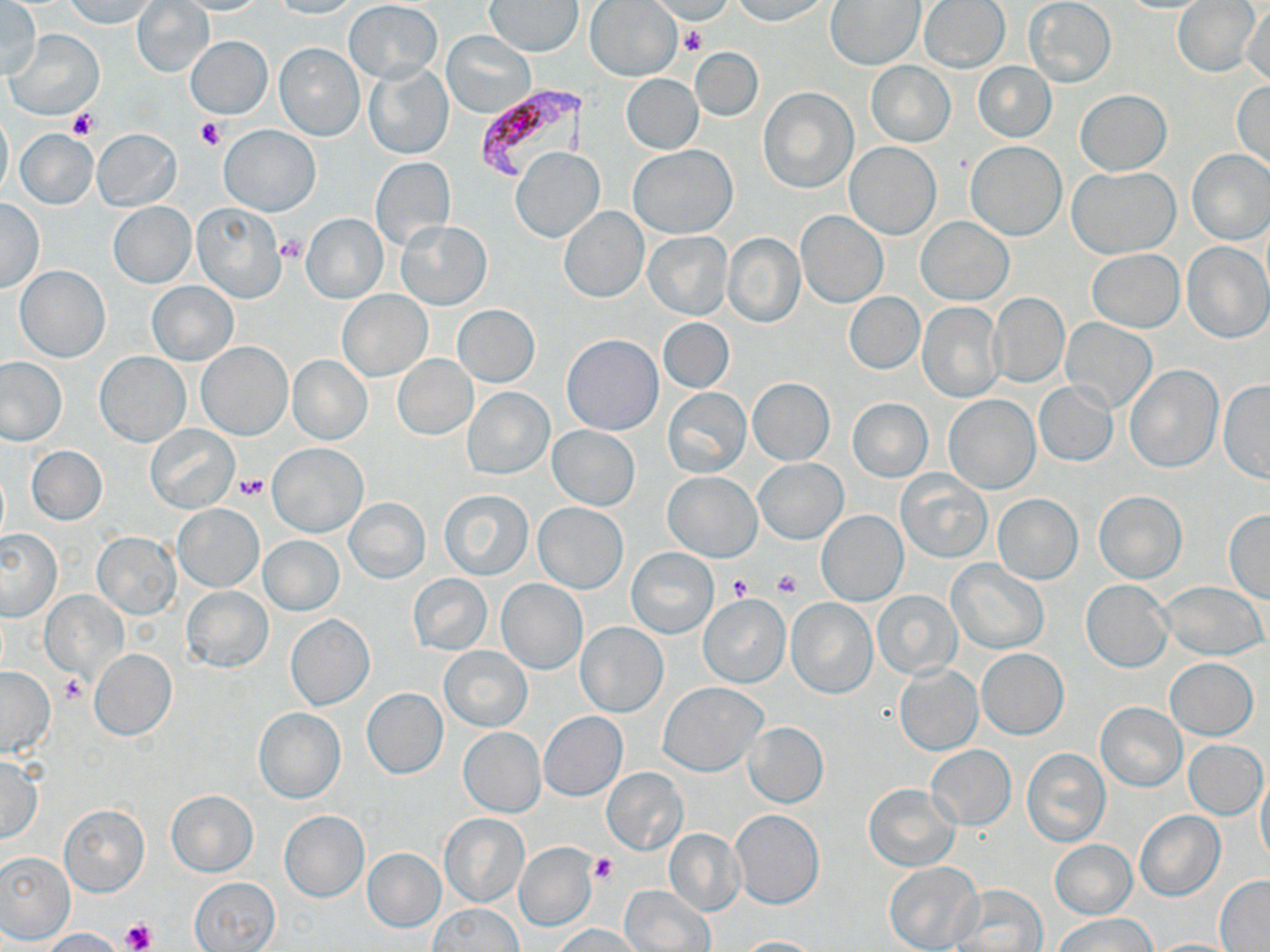

Approximate bounding boxes as (x1, y1, x2, y2) in pixels. Uninfected red blood cell locations: (1, 0, 41, 81), (65, 0, 158, 28), (131, 0, 214, 78), (168, 0, 268, 15), (269, 0, 361, 18), (650, 0, 735, 23), (731, 0, 833, 24), (920, 0, 1009, 71), (1173, 0, 1260, 77), (345, 1, 442, 83), (486, 1, 582, 56), (585, 1, 682, 81), (826, 1, 926, 71), (1024, 1, 1116, 88), (1241, 4, 1270, 87), (7, 29, 103, 120), (442, 30, 535, 118), (185, 36, 272, 119), (274, 43, 365, 141), (691, 47, 763, 121), (866, 61, 955, 147), (972, 61, 1056, 143), (364, 63, 454, 160), (622, 74, 703, 153), (1232, 79, 1270, 174), (759, 87, 857, 193), (1076, 89, 1171, 175), (0, 111, 13, 201), (219, 124, 320, 217), (93, 128, 182, 210), (16, 129, 98, 209), (966, 141, 1067, 240), (845, 142, 942, 240), (629, 145, 737, 238), (511, 147, 605, 243), (1187, 149, 1270, 245), (370, 157, 456, 251), (1068, 166, 1177, 258), (0, 198, 44, 293), (108, 201, 196, 288), (192, 203, 287, 303), (559, 207, 650, 302), (796, 210, 889, 308), (300, 211, 389, 303), (916, 215, 1014, 305), (395, 221, 491, 311), (644, 231, 731, 319), (721, 233, 806, 328), (1183, 242, 1269, 343), (1088, 249, 1184, 332), (14, 266, 110, 362), (146, 279, 238, 366), (338, 290, 432, 381), (844, 293, 924, 374), (990, 294, 1070, 386), (918, 303, 1003, 402), (453, 306, 540, 387), (657, 317, 734, 393), (1060, 319, 1157, 413), (1097, 328, 1205, 451), (562, 334, 663, 435), (197, 342, 291, 440), (96, 352, 190, 447), (392, 354, 477, 441), (288, 356, 372, 444), (0, 358, 66, 445), (1124, 364, 1222, 472), (747, 378, 834, 466), (1218, 381, 1270, 484), (1034, 382, 1117, 467), (463, 387, 554, 479), (663, 388, 751, 477), (943, 394, 1040, 494), (847, 398, 933, 483), (145, 423, 240, 514), (547, 425, 640, 510), (267, 442, 368, 537), (27, 445, 107, 525), (755, 459, 847, 544), (896, 470, 992, 563), (662, 471, 762, 562), (440, 489, 533, 579), (1092, 491, 1187, 583), (991, 494, 1082, 585), (344, 498, 430, 582), (534, 502, 627, 593), (173, 503, 264, 592), (816, 511, 908, 606), (1224, 511, 1270, 602), (0, 530, 63, 621), (93, 532, 180, 618), (258, 534, 344, 615), (627, 547, 718, 638), (947, 559, 1048, 654), (407, 573, 492, 656), (1081, 579, 1173, 672), (497, 580, 588, 675), (1158, 581, 1266, 660), (182, 586, 272, 673), (870, 590, 963, 679), (42, 592, 128, 682), (698, 593, 791, 688), (785, 597, 878, 698), (286, 615, 374, 710), (577, 622, 668, 717), (441, 646, 532, 731), (977, 649, 1068, 739), (90, 650, 176, 740), (1165, 658, 1258, 739), (895, 664, 983, 755), (0, 666, 55, 756), (658, 682, 767, 775), (360, 688, 448, 779), (1096, 703, 1186, 791), (253, 708, 347, 804), (539, 712, 627, 800), (745, 722, 828, 807), (458, 727, 545, 817), (1185, 739, 1267, 819), (927, 746, 1016, 831), (1022, 747, 1110, 847), (0, 755, 43, 843), (601, 768, 689, 855), (1257, 768, 1270, 869), (863, 784, 959, 871), (167, 789, 257, 877), (60, 804, 148, 896), (729, 809, 824, 908), (279, 811, 369, 901), (1135, 812, 1224, 901), (438, 814, 530, 909), (662, 828, 746, 916), (1049, 839, 1138, 919), (515, 845, 596, 930), (361, 848, 447, 932), (1, 851, 75, 943), (883, 861, 982, 952), (190, 877, 280, 950), (1215, 877, 1270, 950), (620, 884, 715, 951), (951, 885, 1048, 952), (426, 903, 523, 952), (1054, 913, 1157, 952), (551, 923, 645, 952), (41, 928, 126, 952), (732, 935, 822, 952), (1146, 939, 1242, 951). Platelet locations: (679, 27, 707, 56), (67, 107, 98, 140), (195, 119, 226, 151), (278, 235, 306, 263), (234, 474, 269, 500), (773, 569, 802, 598), (728, 575, 755, 602), (60, 676, 87, 705), (588, 854, 616, 883), (122, 919, 155, 950). Plasmodium falciparum-infected red blood cell locations: (471, 82, 590, 181). Slide-level diagnosis: Plasmodium falciparum. Image is 1270×952 pixels. Single field of view. May-Grünwald-Giemsa stain. Captured at 1000x magnification. Light microscopy. Thin blood film.